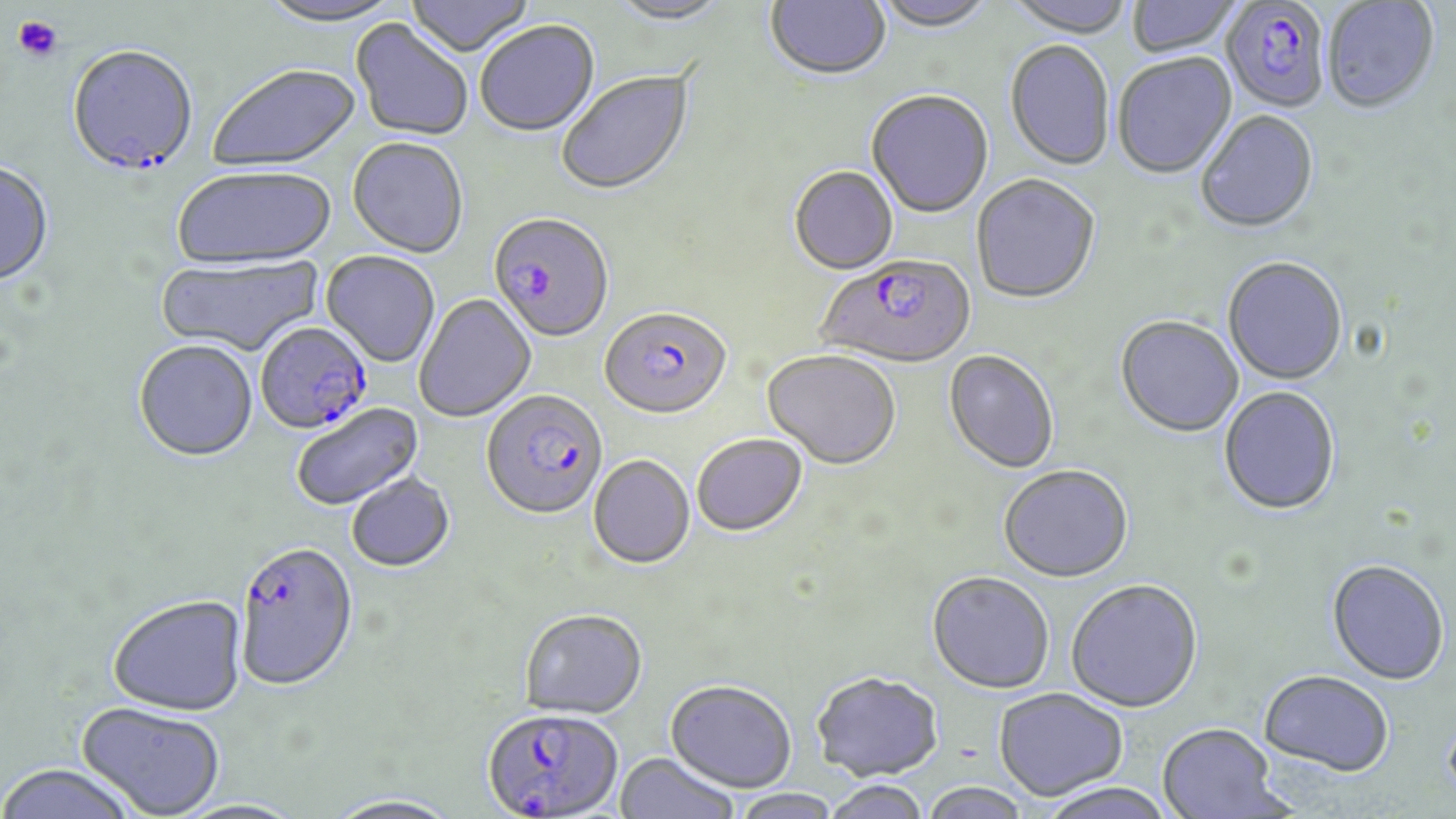
{
  "slide_level_diagnosis": "Plasmodium falciparum",
  "stain": "May-Grünwald-Giemsa",
  "platelet_locations": "approximate bounding boxes as (x1, y1, x2, y2) in pixels: (12, 14, 64, 64)",
  "uninfected_red_blood_cell_locations": "approximate bounding boxes as (x1, y1, x2, y2) in pixels: (258, 0, 407, 29), (405, 0, 534, 59), (606, 0, 731, 27), (765, 0, 893, 84), (1005, 0, 1136, 39), (872, 1, 997, 35), (1126, 1, 1242, 59), (1322, 1, 1440, 115), (350, 18, 474, 142), (475, 21, 600, 138), (1005, 42, 1115, 172), (1113, 54, 1238, 181), (207, 65, 361, 173), (557, 71, 694, 197), (866, 92, 993, 219), (1196, 112, 1319, 235), (347, 138, 468, 259), (0, 163, 55, 289), (172, 168, 336, 272), (789, 168, 898, 276), (970, 175, 1100, 306), (321, 251, 440, 368), (155, 254, 325, 359), (1223, 259, 1348, 386), (415, 294, 537, 423), (1115, 317, 1244, 439), (133, 342, 260, 465), (762, 350, 901, 471), (944, 352, 1059, 474), (1219, 387, 1341, 517), (292, 404, 424, 512), (692, 435, 808, 537), (589, 456, 695, 570), (998, 466, 1134, 584), (346, 474, 456, 573), (1327, 559, 1450, 685), (926, 570, 1055, 694), (1065, 579, 1203, 713), (108, 596, 248, 718), (521, 609, 648, 720), (1258, 669, 1393, 777), (812, 670, 944, 780), (665, 678, 798, 793), (993, 687, 1129, 801), (75, 702, 225, 818), (1157, 722, 1285, 819), (614, 753, 738, 818), (0, 764, 140, 819), (821, 780, 931, 819), (918, 781, 1033, 819), (1039, 781, 1177, 819), (731, 789, 843, 819), (323, 794, 464, 819)",
  "preparation": "thin blood film",
  "field_of_view": "single",
  "plasmodium_falciparum_infected_red_blood_cell_locations": "approximate bounding boxes as (x1, y1, x2, y2) in pixels: (1221, 2, 1331, 115), (66, 48, 199, 180), (488, 214, 615, 344), (817, 257, 977, 371), (600, 309, 732, 422), (255, 324, 374, 436), (481, 390, 608, 522), (234, 543, 359, 693), (480, 707, 624, 819)",
  "magnification": "1000x",
  "modality": "optical microscopy",
  "image_size": "1456×819 pixels"
}